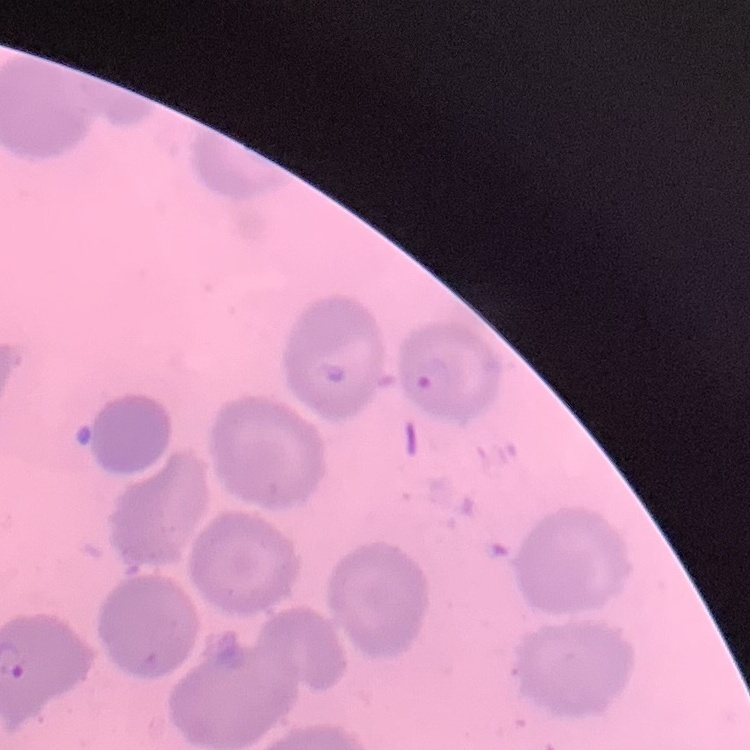

Summary:
  - Red blood cell morphology: no rouleaux formation
  - Preparation: thin blood smear
  - Image type: one tile cut from a larger photomicrograph
  - Stain: Field's or Giemsa